Name the cell type shown.
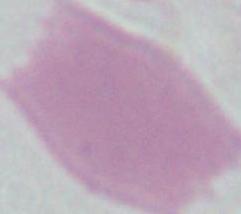

This is an erythrocyte.

Summary:
  - Modality: micrograph
  - Magnification: 1000x